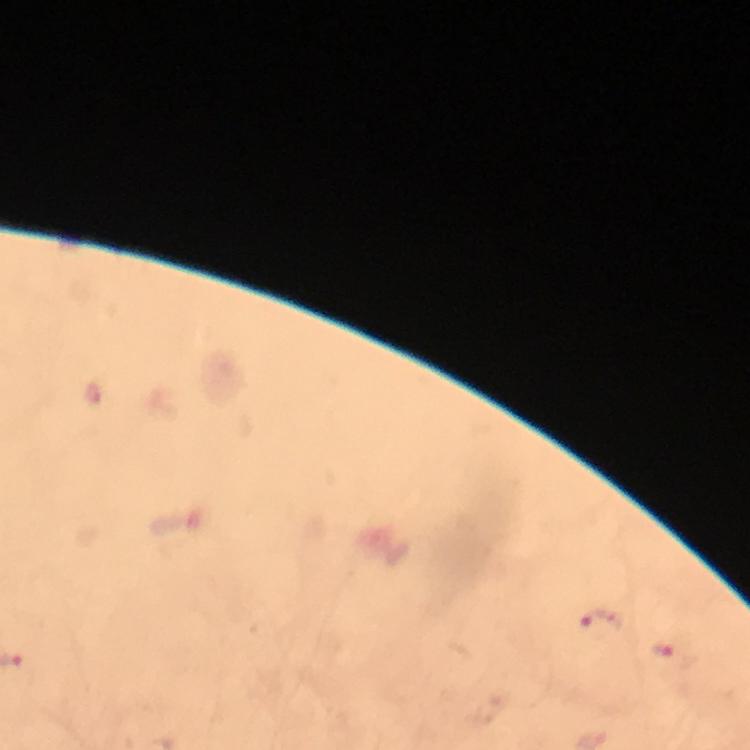

plasmodium_parasite_locations: 'approximate centers as {x, y} in pixels: {599, 623}, {662, 652}'
context: from a diagnostic examination for malaria
image_size: 750×750 pixels
stain: Giemsa
capture: smartphone camera through the microscope
immersion_oil: used
preparation: thick blood film
cropped_from: a single field of view
magnification: 100x